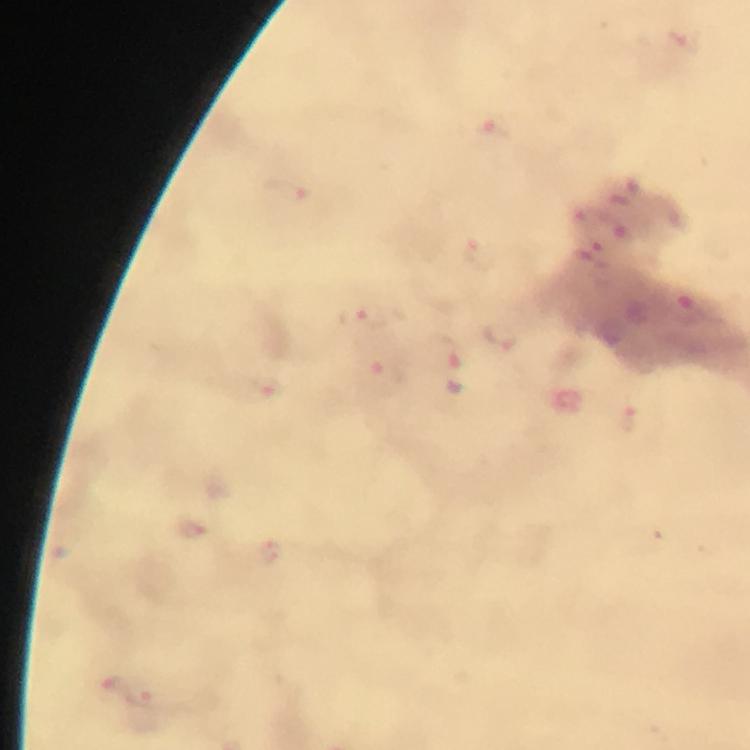 Approximate object centers, in pixels from the top-left corner. Malaria parasite locations: (x=683, y=43), (x=495, y=127), (x=288, y=192), (x=479, y=253), (x=361, y=316), (x=501, y=336), (x=454, y=363), (x=383, y=370), (x=268, y=388), (x=627, y=418), (x=191, y=527), (x=272, y=552), (x=114, y=689), (x=147, y=698). From a diagnostic examination for malaria. Giemsa stain. Immersion oil applied. At 100x magnification. Thick blood film. Photographed through the microscope with a smartphone camera. Image is 750×750 pixels. A crop from one field of view.